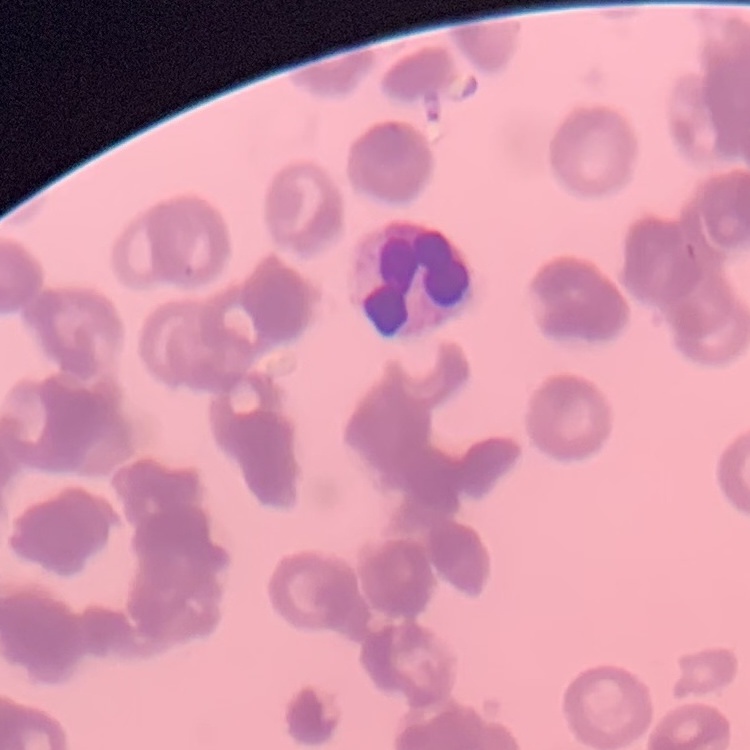
erythrocyte_morphology: rouleaux formation
image_type: square crop of a larger photomicrograph
stain: Field's or Giemsa
preparation: thin blood smear